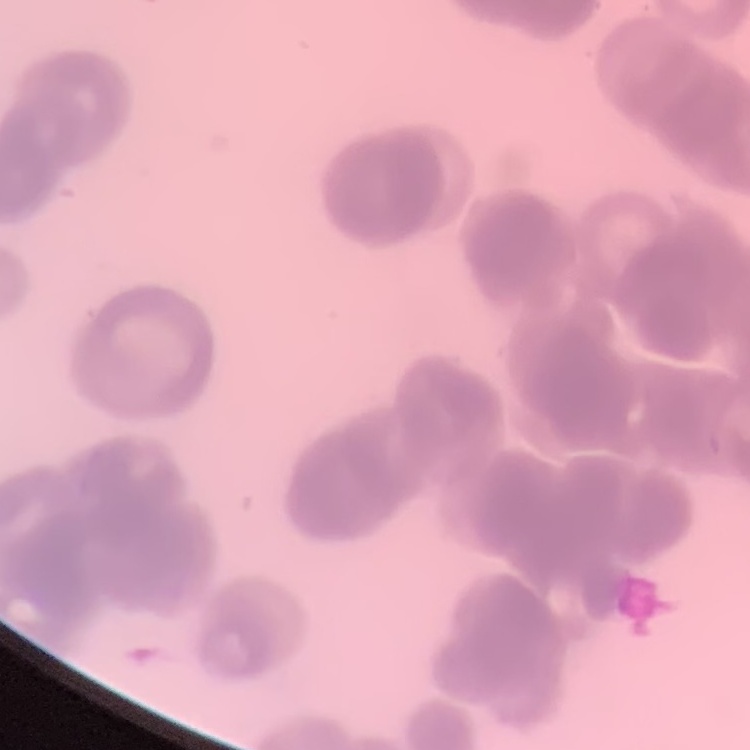

{
  "erythrocyte_morphology": "rouleaux formation",
  "image_type": "one tile cut from a larger photomicrograph",
  "stain": "Field's or Giemsa",
  "preparation": "thin blood smear"
}